Give the position of every Plasmodium parasite.
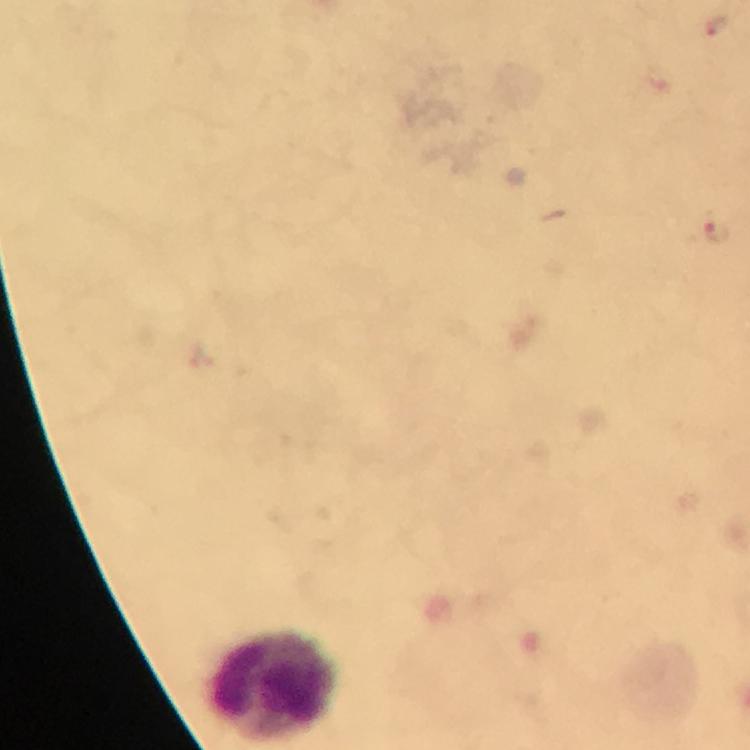

Approximate centers as (x, y) in pixels.
Plasmodium parasites: (716, 26), (717, 228).

Summary:
  - Leukocyte locations: (272, 687)
  - Cropped from: a single field of view
  - Capture: smartphone camera through the microscope
  - Immersion oil: used
  - Preparation: thick blood smear
  - Image size: 750×750 pixels
  - Magnification: 100x
  - Context: from a malaria diagnostic workup
  - Stain: Giemsa